Identify the cell.
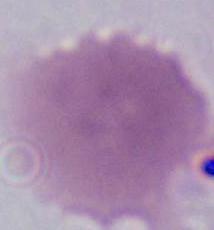
This is an erythrocyte.

Summary:
  - Modality: photomicrograph
  - Magnification: 1000x